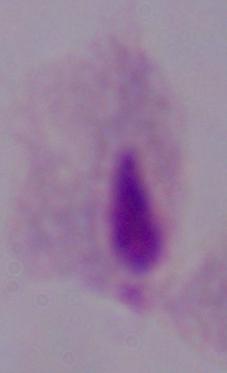

Summary:
  - Magnification: 1000x
  - Identification: trichomonad
  - Modality: micrograph